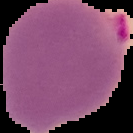
Segmented cell region on a black background. From a thin blood film. Image is 133×133 pixels. Malaria status: parasitized.